Classify this cell by malaria status.
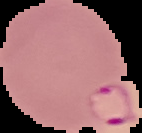

Parasitized.

Summary:
  - Image type: segmented cell region on a black background
  - Image size: 142×133 pixels
  - Preparation: thin blood smear